Classify this cell by malaria status.
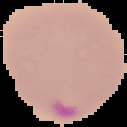

Parasitized.

Summary:
  - Image size: 127×127 pixels
  - Preparation: thin blood film
  - Image type: cell region segmented out of the field of view; surrounding area masked to black